Assess the morphology of the erythrocytes.
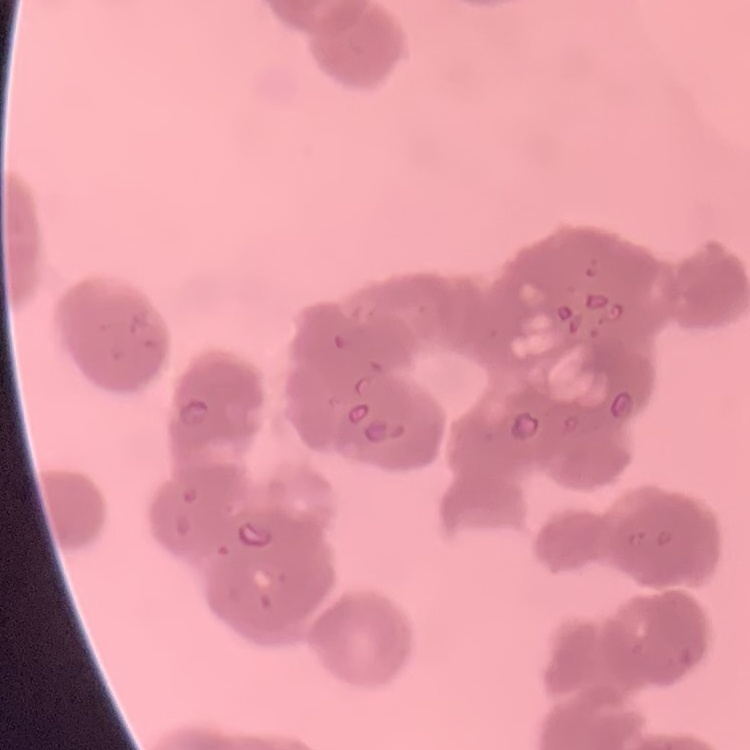

They show rouleaux formation.

preparation = thin peripheral smear
image type = one tile cut from a larger photomicrograph
stain = Field's or Giemsa